Report the malaria status of this cell.
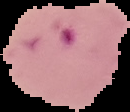

Parasitized.

image_type: segmented cell region with the area outside set to black
image_size: 130×112 pixels
preparation: thin blood smear